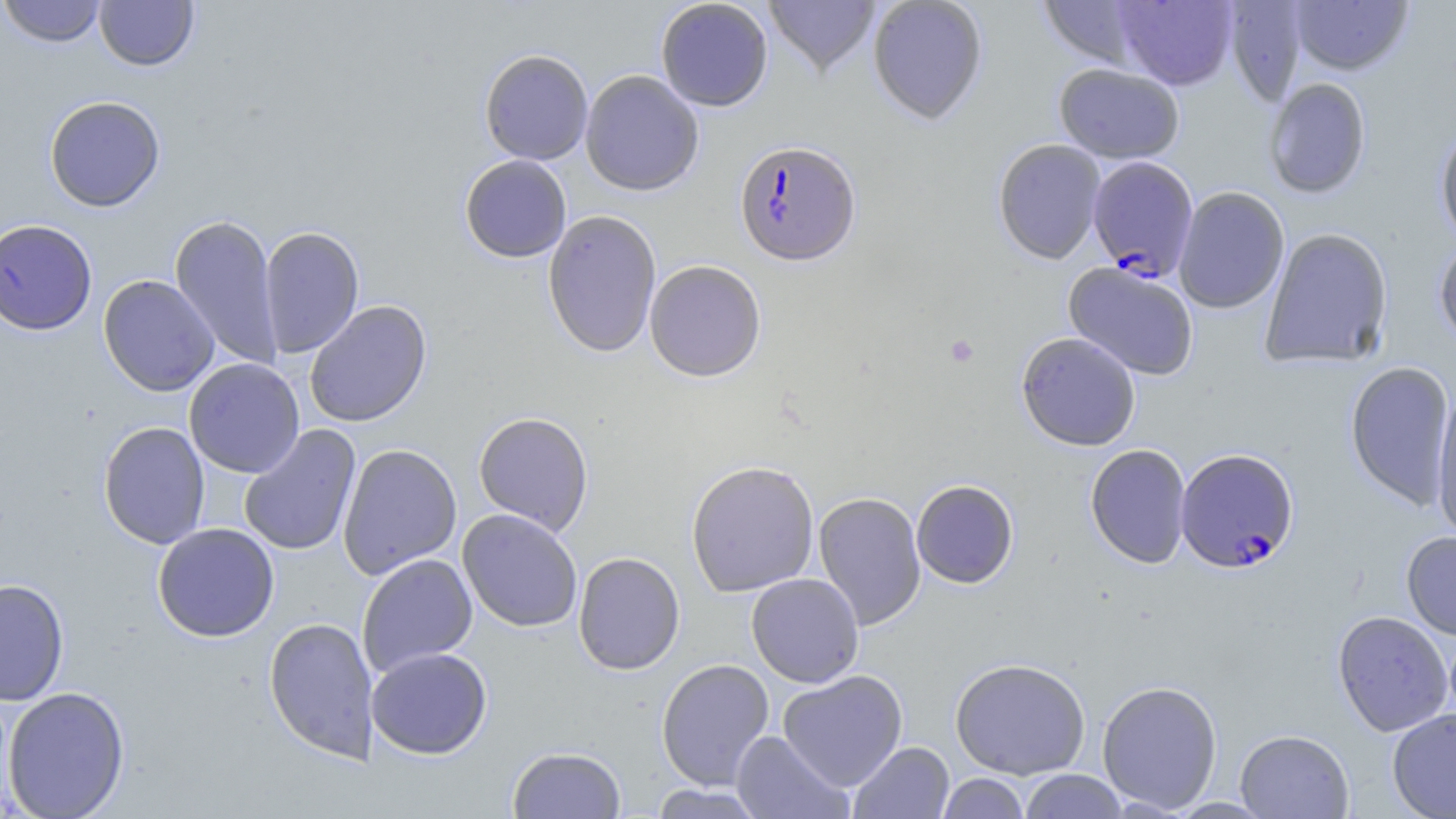
Summary:
  - Coordinate format: approximate bounding boxes as named x1/y1/x2/y2 corners in pixels
  - Platelet locations: (x1=944, y1=335, x2=980, y2=368)
  - Plasmodium falciparum-infected red blood cell locations: (x1=737, y1=144, x2=864, y2=271), (x1=1086, y1=155, x2=1199, y2=281), (x1=1175, y1=447, x2=1300, y2=573)
  - Uninfected red blood cell locations: (x1=0, y1=0, x2=106, y2=48), (x1=94, y1=0, x2=198, y2=71), (x1=655, y1=0, x2=773, y2=112), (x1=763, y1=0, x2=880, y2=78), (x1=867, y1=0, x2=987, y2=125), (x1=1111, y1=0, x2=1238, y2=90), (x1=1037, y1=1, x2=1150, y2=69), (x1=1287, y1=1, x2=1413, y2=75), (x1=1223, y1=3, x2=1308, y2=106), (x1=480, y1=48, x2=593, y2=165), (x1=1054, y1=63, x2=1184, y2=163), (x1=580, y1=69, x2=704, y2=196), (x1=1262, y1=78, x2=1372, y2=198), (x1=44, y1=95, x2=165, y2=212), (x1=1434, y1=124, x2=1456, y2=250), (x1=992, y1=138, x2=1106, y2=264), (x1=459, y1=155, x2=572, y2=263), (x1=1173, y1=187, x2=1290, y2=314), (x1=542, y1=209, x2=662, y2=358), (x1=169, y1=213, x2=284, y2=370), (x1=2, y1=219, x2=99, y2=335), (x1=259, y1=225, x2=365, y2=358), (x1=1259, y1=227, x2=1394, y2=369), (x1=1433, y1=238, x2=1456, y2=351), (x1=644, y1=259, x2=767, y2=382), (x1=1063, y1=262, x2=1200, y2=381), (x1=98, y1=274, x2=219, y2=396), (x1=304, y1=300, x2=432, y2=428), (x1=1016, y1=332, x2=1141, y2=451), (x1=184, y1=358, x2=305, y2=478), (x1=1345, y1=360, x2=1455, y2=510), (x1=1431, y1=387, x2=1456, y2=545), (x1=473, y1=411, x2=593, y2=535), (x1=98, y1=420, x2=210, y2=549), (x1=239, y1=425, x2=362, y2=556), (x1=1084, y1=443, x2=1192, y2=569), (x1=337, y1=444, x2=462, y2=579), (x1=685, y1=459, x2=820, y2=597), (x1=911, y1=480, x2=1018, y2=588), (x1=813, y1=491, x2=927, y2=630), (x1=458, y1=509, x2=583, y2=633), (x1=152, y1=522, x2=280, y2=642), (x1=1401, y1=531, x2=1456, y2=640), (x1=573, y1=551, x2=685, y2=675), (x1=357, y1=553, x2=477, y2=677), (x1=746, y1=573, x2=864, y2=687), (x1=1, y1=578, x2=70, y2=706), (x1=1332, y1=610, x2=1454, y2=737), (x1=263, y1=616, x2=378, y2=764), (x1=366, y1=647, x2=492, y2=759), (x1=656, y1=658, x2=775, y2=791), (x1=950, y1=658, x2=1091, y2=779), (x1=778, y1=670, x2=908, y2=791), (x1=1096, y1=679, x2=1222, y2=812), (x1=3, y1=686, x2=130, y2=818), (x1=1387, y1=708, x2=1456, y2=818), (x1=1235, y1=729, x2=1354, y2=818), (x1=731, y1=731, x2=854, y2=819), (x1=848, y1=742, x2=954, y2=819), (x1=507, y1=746, x2=627, y2=818), (x1=1019, y1=769, x2=1128, y2=818), (x1=936, y1=773, x2=1031, y2=818), (x1=648, y1=784, x2=769, y2=818)
  - Slide-level diagnosis: Plasmodium falciparum
  - Field of view: one of a larger specimen
  - Magnification: 1000x
  - Stain: May-Grünwald-Giemsa
  - Modality: optical microscopy
  - Preparation: thin blood smear
  - Image size: 1456×819 pixels